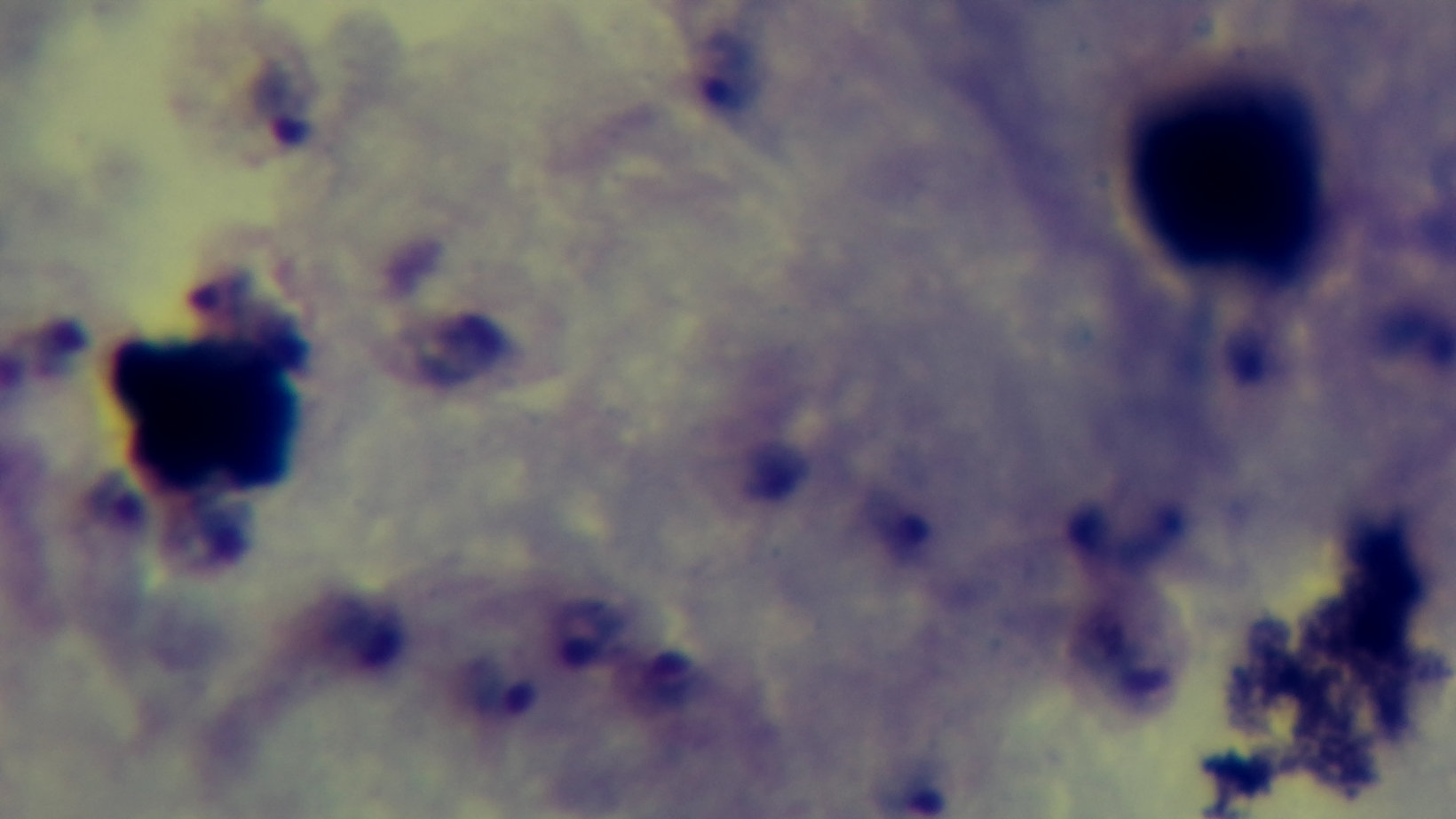
Summary:
  - Objective: 100x oil immersion
  - Stain: Giemsa
  - Malaria status: infected
  - Modality: light microscopy
  - Capture: mounted 4K digital camera
  - Preparation: thick blood film
  - Field of view: single